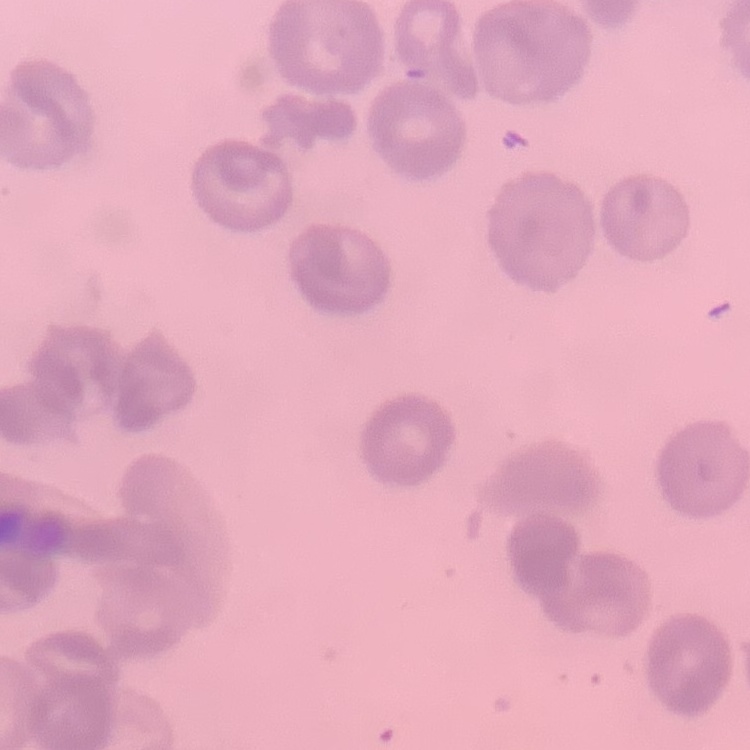

The erythrocytes exhibit no rouleaux formation. One tile cut from a larger photomicrograph. Thin blood film. Field's or Giemsa stain.